Give the extent of the malaria parasites you find, grouped by life-cycle stage — ring form, trophozoite, schizont, or gametocyte.
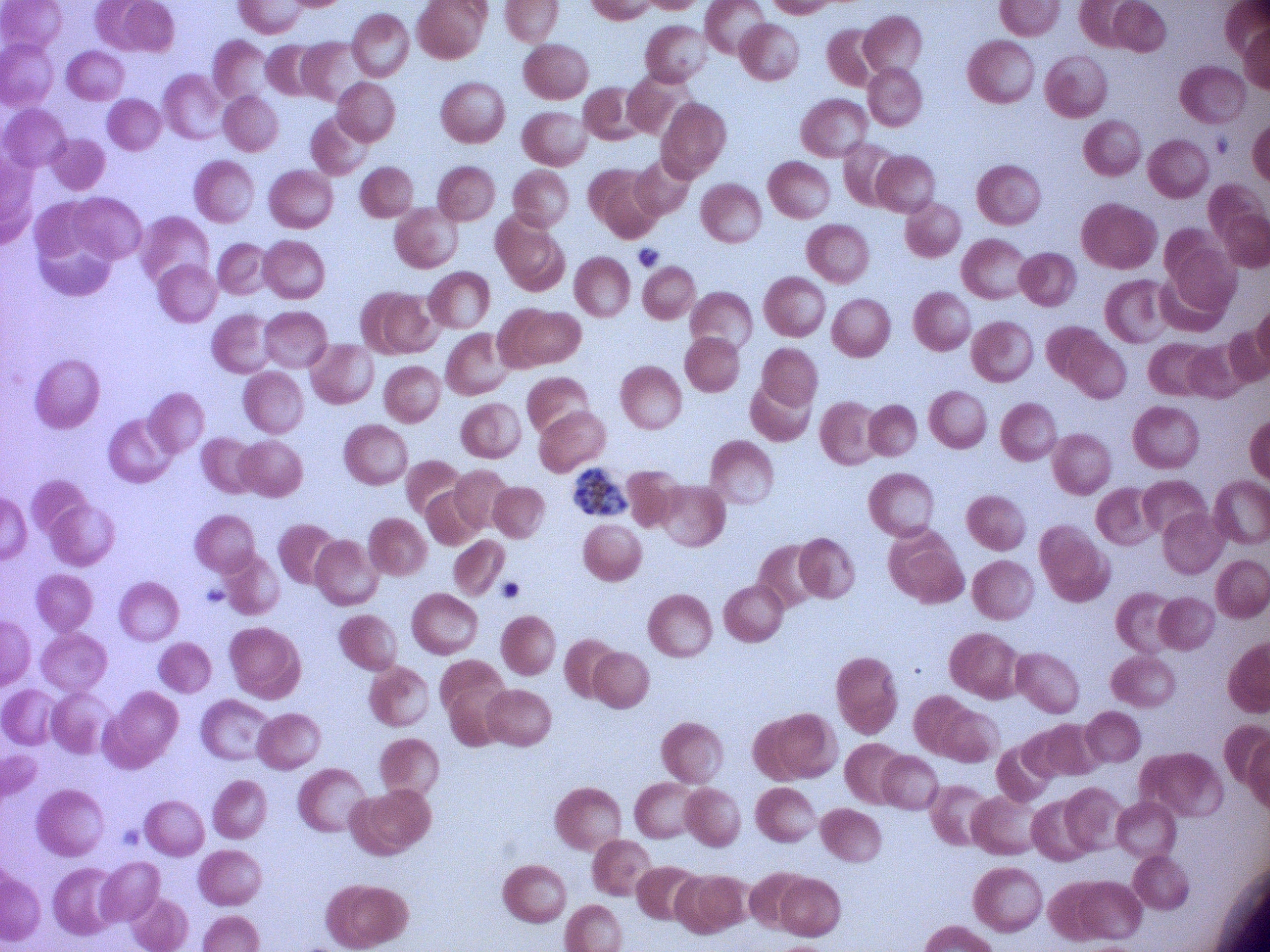
Approximate bounding boxes as (x1, y1, x2, y2) in pixels, from the source annotation, which is not necessarily exhaustive.
Schizonts: (574, 466, 628, 515).

{
  "microscope": "Leica DM2000 with built-in camera",
  "image_size": "1270×952 pixels",
  "magnification": "100x",
  "preparation": "thin blood smear",
  "field_of_view": "one from this slide",
  "species": "Plasmodium falciparum",
  "stain": "Giemsa"
}